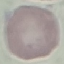
Malaria status: uninfected. Thin blood smear. Giemsa-stained preparation. Acquired by smartphone through the microscope eyepiece. Automatically extracted cell patch, resized to 64 × 64 pixels.